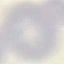

Malaria status: uninfected. Thin smear of blood. Automatically extracted cell patch, resized to 64 × 64 pixels. Photographed with a smartphone camera at the microscope eyepiece. Giemsa stain.